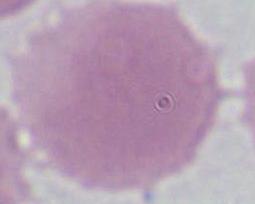 Captured at 1000x magnification. Photomicrograph. An erythrocyte is seen.